State which cell type is depicted.
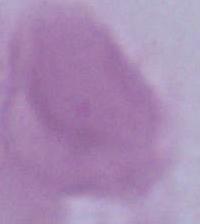

This is an erythrocyte.

Summary:
  - Modality: micrograph
  - Magnification: 1000x